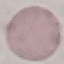
{
  "malaria_status": "uninfected",
  "capture": "smartphone camera at the microscope eyepiece",
  "preparation": "thin blood film",
  "image_type": "automatically extracted cell patch, resized to 64 × 64 pixels",
  "stain": "Giemsa"
}